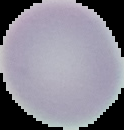

From a thin blood smear. The area outside the segmented cell region is set to black. Image is 124×130 pixels. Result: negative for Plasmodium parasites.